Report the malaria status of this cell.
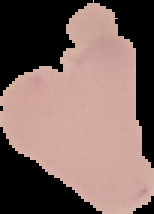
Uninfected.

Summary:
  - Preparation: thin blood smear
  - Image type: cell region segmented out of the field of view; surrounding area masked to black
  - Image size: 154×214 pixels